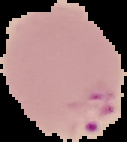

image size = 127×142 pixels
preparation = thin blood film
image type = cell region segmented out of the field of view; surrounding area masked to black
result = malaria parasites detected